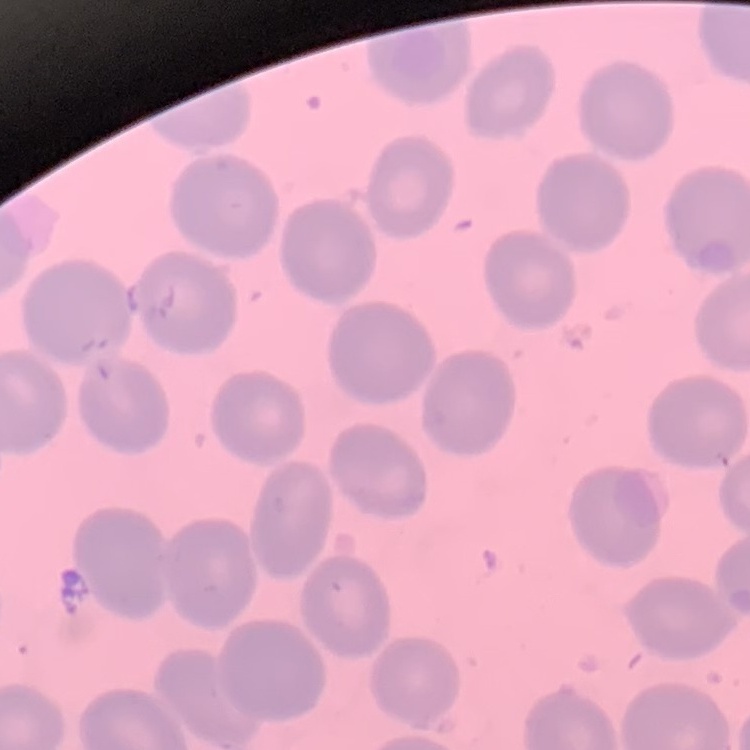
Summary:
  - Red blood cell morphology: no rouleaux formation
  - Preparation: thin blood smear
  - Stain: Field's or Giemsa
  - Image type: one tile cut from a larger photomicrograph